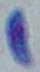 Micrograph. Captured at 1000x magnification. Toxoplasma gondii is seen.